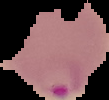
Summary:
  - Result: Plasmodium parasites identified
  - Preparation: thin blood film
  - Image type: cell region segmented out of the field of view; surrounding area masked to black
  - Image size: 109×100 pixels